State which cell type is depicted.
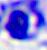

A leukocyte.

Micrograph. 400x magnification.